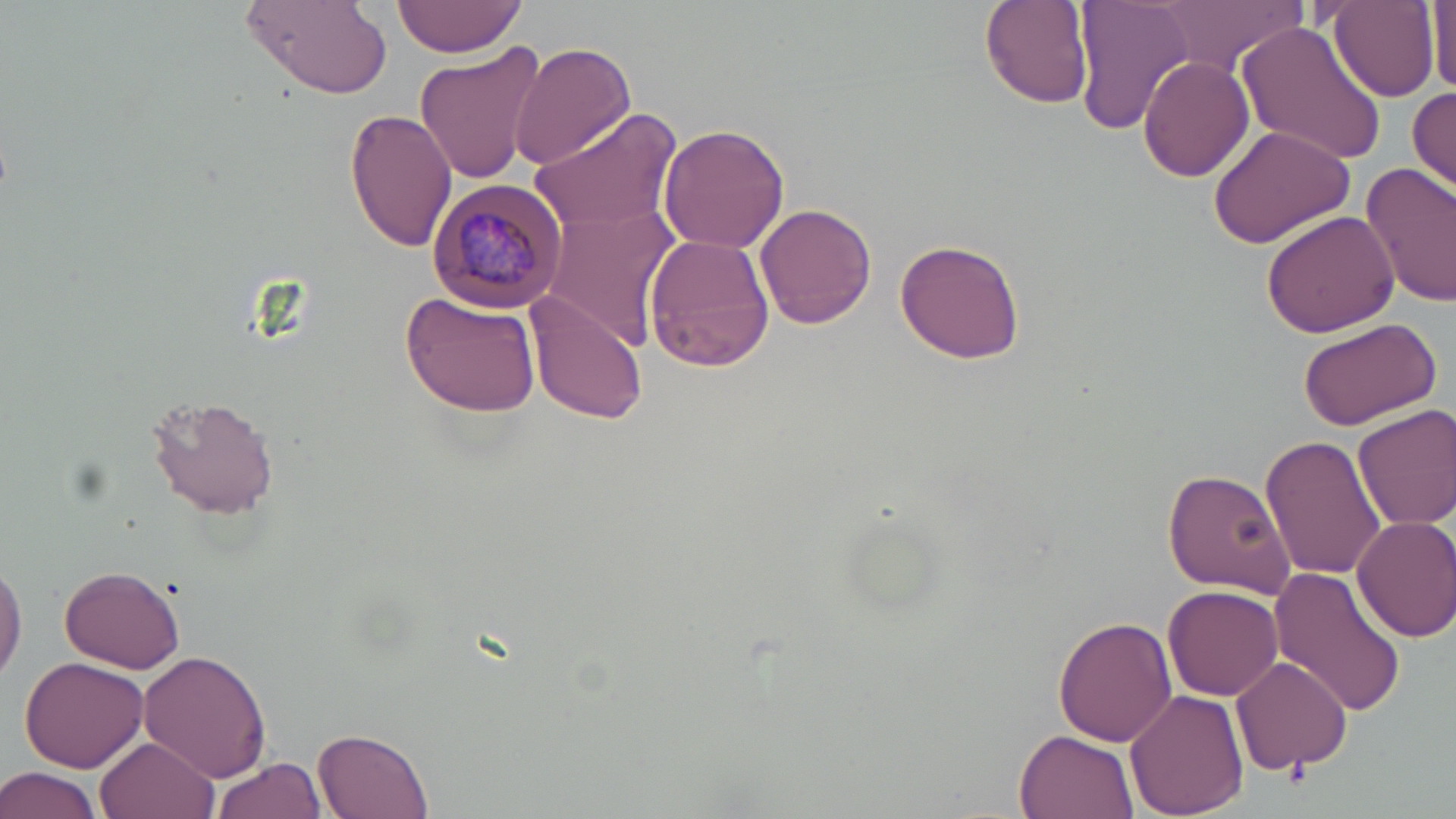

Approximate bounding boxes as (x1,y1)-(x2,y2) corner pairs in pixels. Uninfected red blood cell locations: (240,0)-(394,97), (394,0)-(530,58), (979,0)-(1093,108), (1073,0)-(1198,133), (1156,0)-(1304,80), (1325,0)-(1439,102), (1428,4)-(1455,97), (1236,22)-(1388,168), (411,37)-(550,185), (510,42)-(635,172), (1139,55)-(1254,182), (1409,86)-(1456,193), (345,107)-(458,253), (528,109)-(684,232), (1207,121)-(1357,249), (658,123)-(790,253), (1361,163)-(1456,309), (539,203)-(681,349), (755,204)-(878,329), (1260,209)-(1400,339), (645,234)-(774,372), (894,237)-(1026,363), (400,290)-(542,419), (525,293)-(651,425), (1297,316)-(1442,430), (147,394)-(279,518), (1351,403)-(1456,532), (1259,434)-(1386,581), (1162,467)-(1296,599), (1350,514)-(1456,643), (0,550)-(26,688), (59,564)-(187,674), (1267,569)-(1407,719), (1165,583)-(1284,700), (1053,616)-(1178,746), (139,651)-(271,780), (20,654)-(148,772), (1229,655)-(1355,773), (1125,688)-(1249,817), (311,725)-(437,818), (1014,729)-(1138,819), (95,736)-(217,819), (210,757)-(328,819), (0,764)-(105,819). Plasmodium malariae-infected red blood cell locations: (427,177)-(570,314). Platelet locations: (1284,761)-(1310,788). Slide-level diagnosis: Plasmodium malariae. Thin blood smear. Image is 1456×819 pixels. 1000x magnification. Optical microscopy. Single field of view. May-Grünwald-Giemsa-stained preparation.